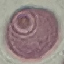

{
  "malaria_status": "uninfected",
  "stain": "Giemsa",
  "image_type": "cell patch, automatically extracted from a larger field of view and resized to 64 × 64 pixels",
  "capture": "smartphone camera at the microscope eyepiece",
  "preparation": "thin blood film"
}